Name the parasite shown.
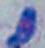
This is Toxoplasma gondii.

Micrograph. 1000x magnification.